Give the position of every leukocyte.
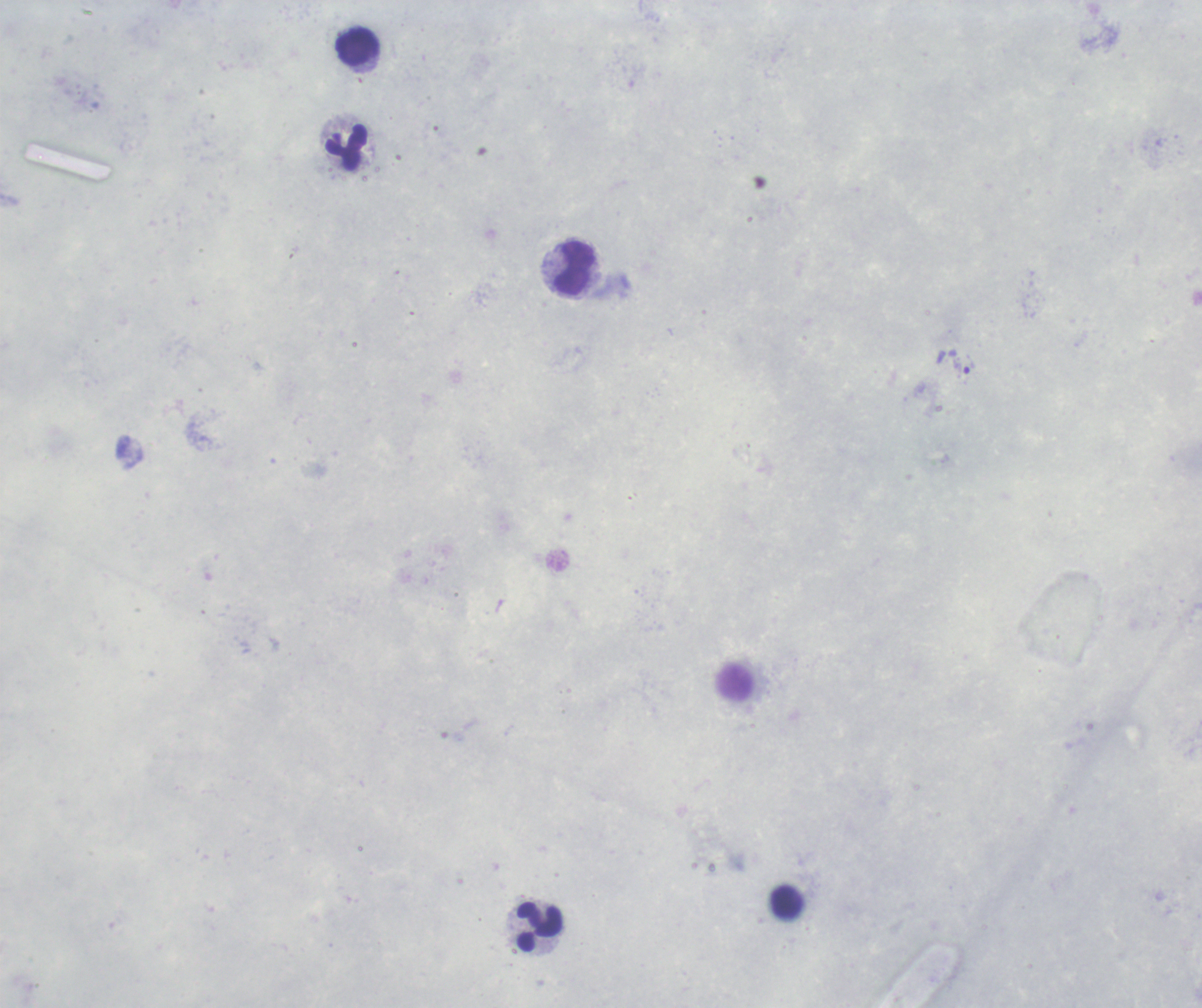
Approximate centers as (x, y) in pixels.
Leukocytes: (358, 49), (347, 148), (575, 269), (734, 682), (788, 904), (539, 927).

Approximate centers as (x, y) in pixels. Trophozoite locations: (964, 365). Background quality: unsatisfactory. Previously used in an actual diagnosis. Romanowsky stain. Captured at 100x magnification. Image is 1202×1008 pixels. Thick blood smear. One field from this slide. Result: malaria parasites detected.